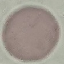

Malaria status: uninfected. Photographed with a smartphone camera at the microscope eyepiece. Automatically extracted cell patch, resized to 64 × 64 pixels. Giemsa-stained preparation. Thin blood smear.